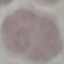
Malaria status: uninfected. Thin blood smear. Automatically extracted cell patch, resized to 64 × 64 pixels. Giemsa-stained preparation. Photographed with a smartphone camera at the microscope eyepiece.